Describe the morphology of the red blood cells.
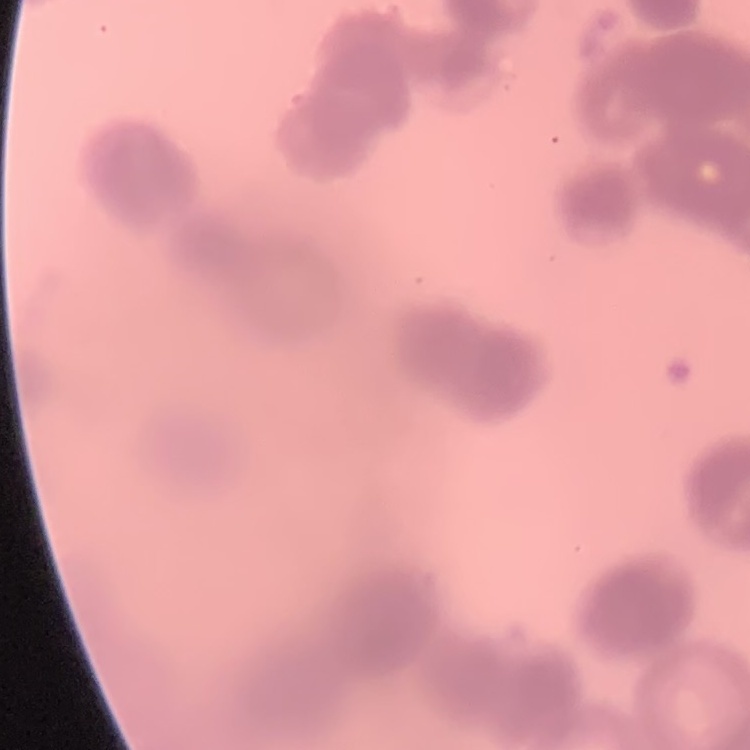
They show rouleaux formation.

preparation = thin peripheral smear
stain = Field's or Giemsa
image type = one tile cut from a larger photomicrograph